Comment on the morphology of the red blood cells.
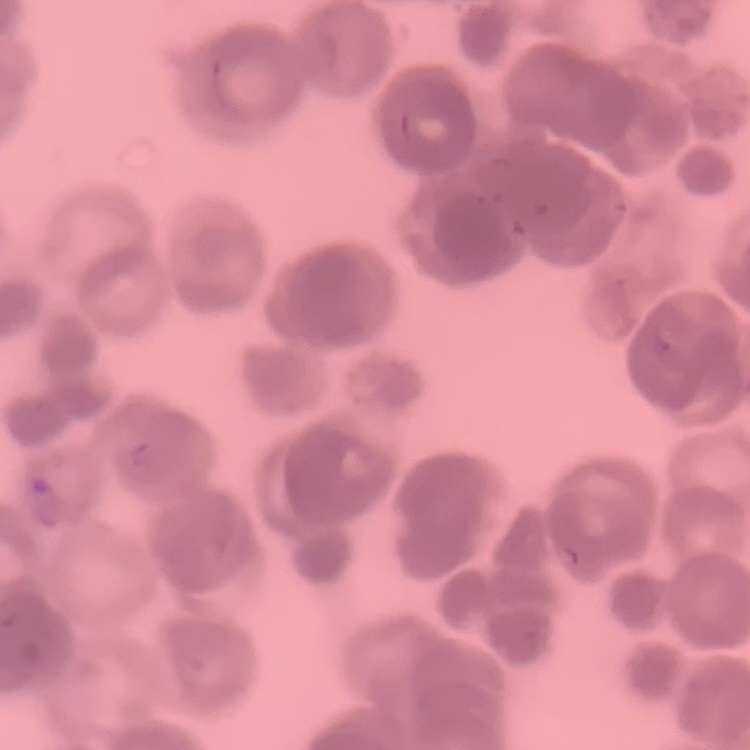
They show rouleaux formation.

Summary:
  - Image type: square crop of a larger photomicrograph
  - Stain: Field's or Giemsa
  - Preparation: thin peripheral smear